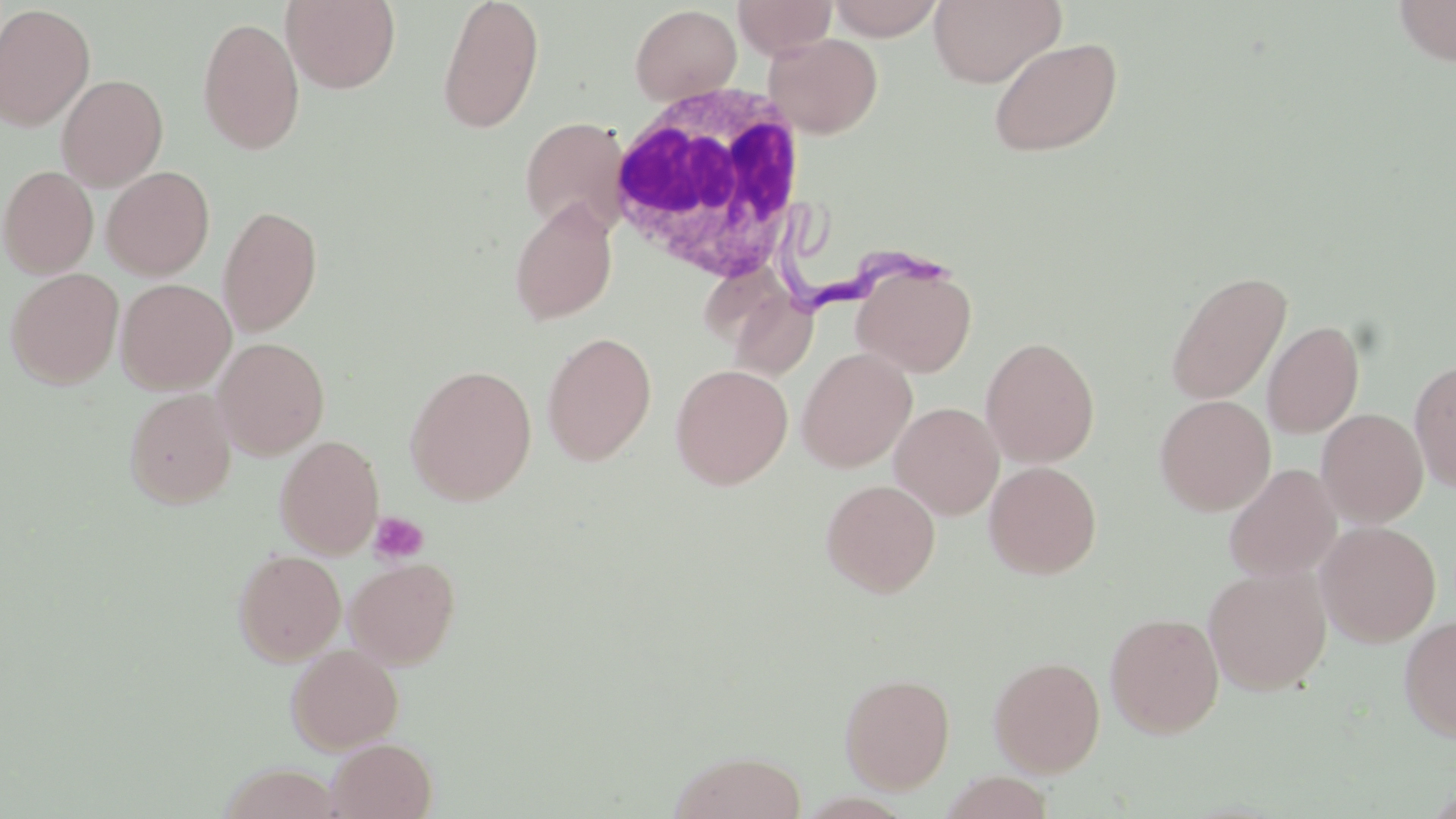
Summary:
  - Coordinate format: approximate bounding boxes as [x1, y1, x2, y2] in pixels
  - White blood cell locations: [599, 82, 812, 285]
  - Uninfected red blood cell locations: [281, 0, 401, 93], [436, 0, 545, 135], [733, 0, 837, 59], [826, 0, 946, 40], [929, 0, 1066, 89], [1392, 0, 1456, 67], [0, 3, 95, 131], [630, 4, 742, 105], [196, 16, 305, 155], [763, 33, 883, 138], [988, 36, 1123, 157], [56, 74, 168, 191], [519, 116, 630, 235], [1, 165, 99, 279], [102, 166, 215, 280], [509, 200, 617, 325], [217, 204, 323, 337], [853, 263, 976, 377], [5, 267, 124, 390], [1165, 269, 1291, 406], [116, 278, 236, 394], [733, 294, 828, 367], [1262, 320, 1364, 439], [542, 331, 657, 466], [981, 336, 1100, 468], [211, 337, 329, 460], [797, 347, 917, 471], [1408, 358, 1456, 494], [404, 363, 538, 505], [670, 363, 793, 489], [124, 388, 238, 508], [1155, 394, 1276, 516], [889, 401, 1005, 519], [1316, 408, 1428, 527], [275, 435, 385, 558], [984, 461, 1102, 578], [1223, 464, 1341, 581], [820, 479, 940, 597], [1316, 520, 1441, 647], [232, 549, 346, 665], [345, 558, 461, 669], [1203, 564, 1332, 695], [1104, 611, 1225, 738], [1398, 615, 1456, 743], [286, 644, 403, 754], [988, 655, 1106, 775], [840, 672, 956, 793], [327, 738, 437, 819], [668, 749, 808, 818], [219, 764, 342, 819], [940, 772, 1054, 819]
  - Platelet locations: [369, 511, 428, 564]
  - Trypanosoma brucei locations: [780, 210, 955, 312]
  - Slide-level diagnosis: Trypanosoma brucei
  - Magnification: 1000x
  - Field of view: single
  - Modality: light microscopy
  - Stain: May-Grünwald-Giemsa
  - Preparation: thin blood film
  - Image size: 1456×819 pixels